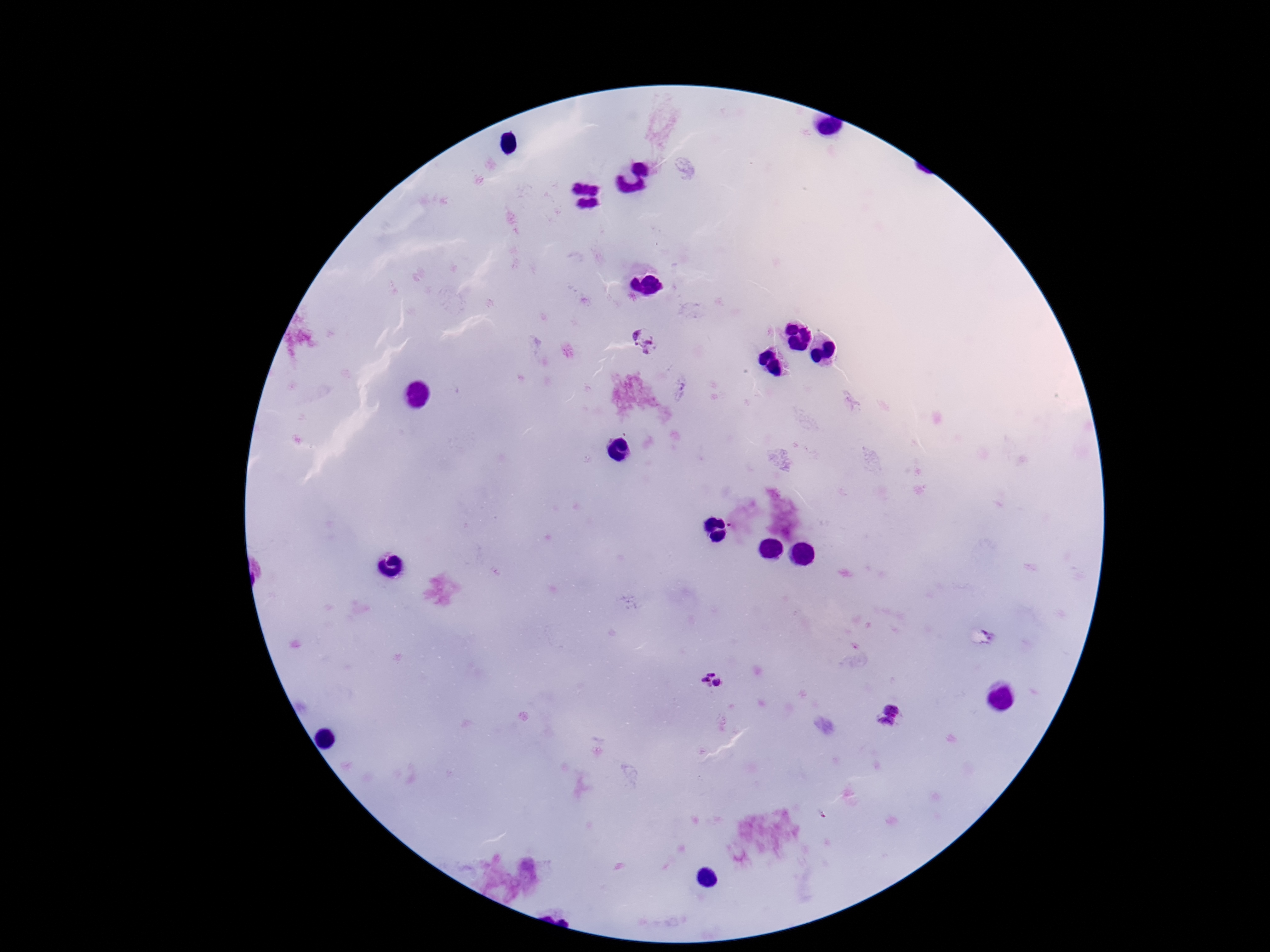
Approximate centers as {x, y} in pixels. Plasmodium parasite locations: {644, 341}, {682, 389}, {710, 682}, {890, 718}. 100x magnification. Image is 1270×952 pixels. Smartphone photograph taken through the microscope eyepiece. Thick blood film. Giemsa stain. Patient malaria status: infected. One field from this slide.